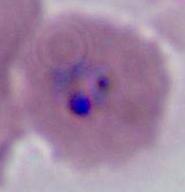
Summary:
  - Modality: photomicrograph
  - Magnification: 400x or 1000x
  - Identification: Plasmodium